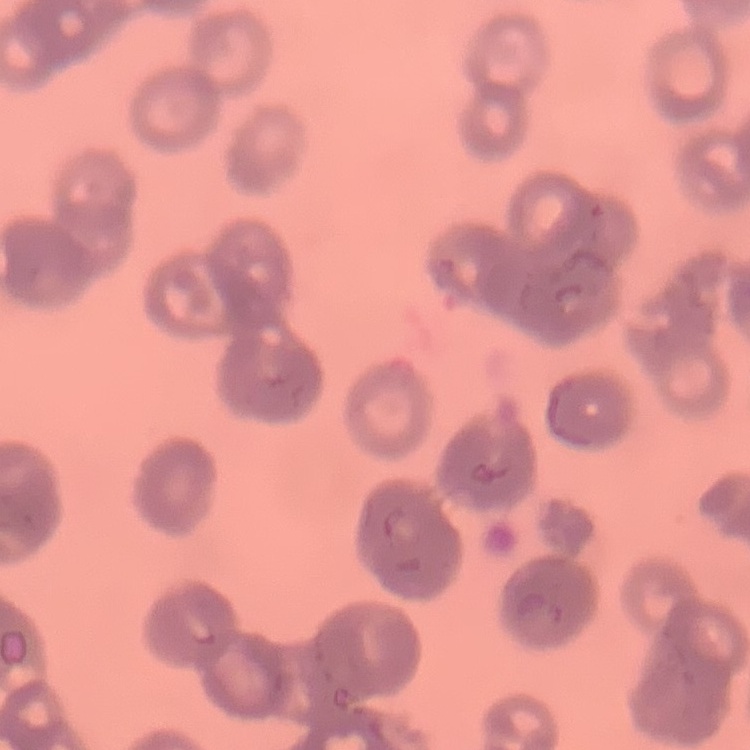
Summary:
  - Red blood cell morphology: rouleaux formation
  - Preparation: thin peripheral smear
  - Image type: square crop of a larger photomicrograph
  - Stain: Field's or Giemsa